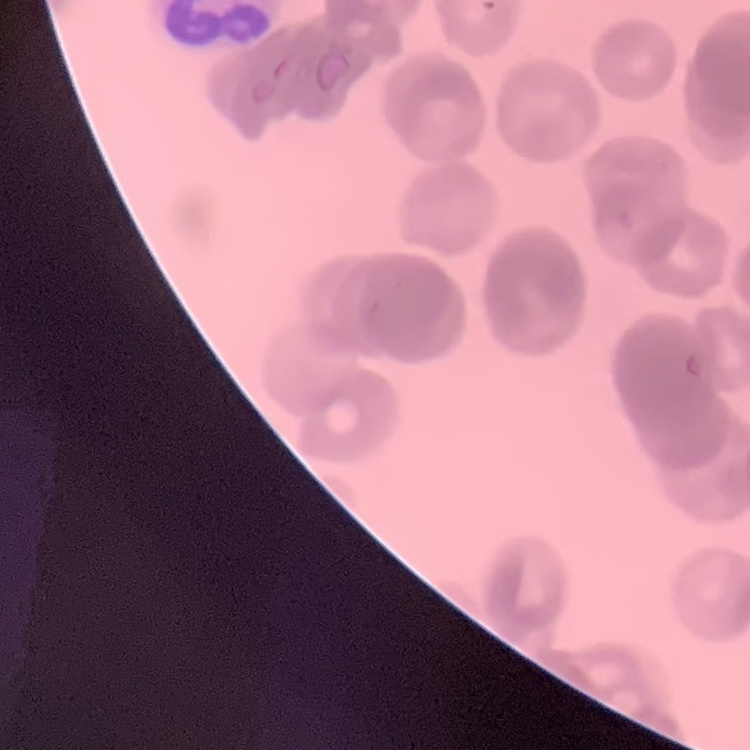 The red blood cells show rouleaux formation. Thin peripheral smear. Stained with either Field's or Giemsa. Square crop of a larger photomicrograph.